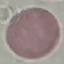
Malaria status: uninfected. Acquired by smartphone through the microscope eyepiece. Cell patch, automatically extracted from a larger field of view and resized to 64 × 64 pixels. Giemsa stain. Thin blood smear.